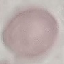
Summary:
  - Result: negative for malaria parasites
  - Stain: Giemsa
  - Image type: cell patch, automatically extracted from a larger field of view and resized to 64 × 64 pixels
  - Capture: smartphone camera at the microscope eyepiece
  - Preparation: thin blood film